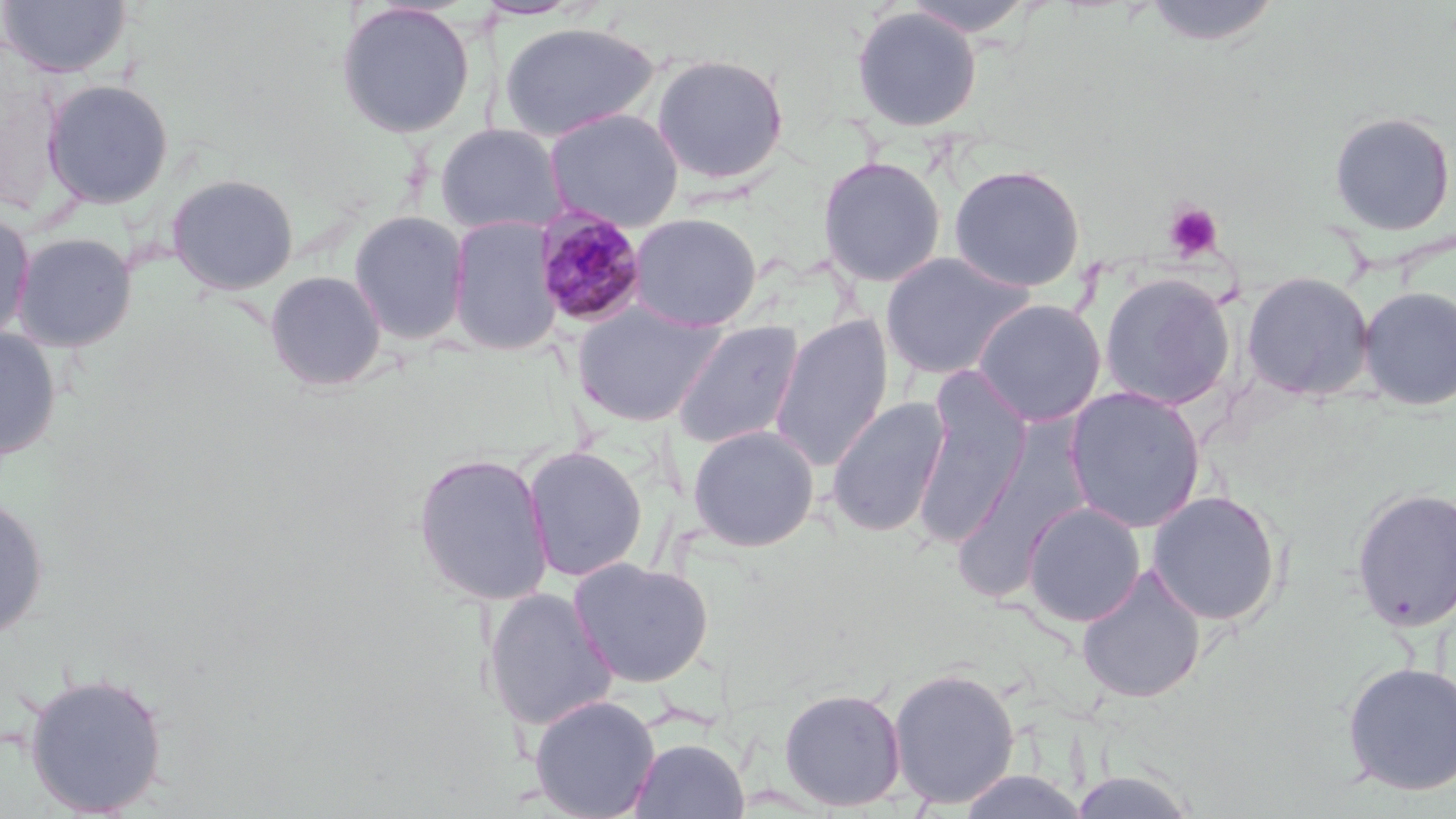

Summary:
  - Coordinate format: approximate bounding boxes as named x1/y1/x2/y2 corners in pixels
  - Platelet locations: (x1=1163, y1=202, x2=1223, y2=261)
  - Plasmodium malariae-infected red blood cell locations: (x1=534, y1=207, x2=648, y2=328)
  - Uninfected red blood cell locations: (x1=0, y1=0, x2=131, y2=78), (x1=899, y1=0, x2=1037, y2=38), (x1=1141, y1=0, x2=1283, y2=47), (x1=334, y1=2, x2=477, y2=139), (x1=851, y1=6, x2=982, y2=132), (x1=497, y1=21, x2=661, y2=142), (x1=651, y1=53, x2=790, y2=186), (x1=42, y1=78, x2=175, y2=209), (x1=544, y1=108, x2=684, y2=232), (x1=1328, y1=111, x2=1455, y2=236), (x1=434, y1=123, x2=568, y2=236), (x1=817, y1=155, x2=946, y2=287), (x1=949, y1=164, x2=1086, y2=292), (x1=166, y1=173, x2=300, y2=295), (x1=0, y1=209, x2=36, y2=347), (x1=348, y1=209, x2=470, y2=346), (x1=628, y1=212, x2=763, y2=331), (x1=447, y1=214, x2=563, y2=355), (x1=11, y1=231, x2=138, y2=353), (x1=879, y1=251, x2=1034, y2=381), (x1=264, y1=270, x2=388, y2=392), (x1=1241, y1=271, x2=1375, y2=401), (x1=1099, y1=273, x2=1236, y2=410), (x1=1358, y1=285, x2=1456, y2=410), (x1=972, y1=298, x2=1107, y2=427), (x1=571, y1=301, x2=724, y2=427), (x1=770, y1=315, x2=894, y2=471), (x1=670, y1=320, x2=805, y2=450), (x1=0, y1=328, x2=61, y2=462), (x1=911, y1=381, x2=1030, y2=547), (x1=1064, y1=387, x2=1205, y2=532), (x1=826, y1=397, x2=950, y2=537), (x1=687, y1=424, x2=821, y2=551), (x1=522, y1=445, x2=648, y2=582), (x1=949, y1=445, x2=1089, y2=602), (x1=411, y1=451, x2=554, y2=607), (x1=1351, y1=486, x2=1456, y2=633), (x1=1147, y1=490, x2=1283, y2=626), (x1=0, y1=494, x2=49, y2=640), (x1=1023, y1=501, x2=1145, y2=627), (x1=568, y1=557, x2=715, y2=688), (x1=1075, y1=565, x2=1207, y2=703), (x1=481, y1=587, x2=618, y2=732), (x1=1341, y1=660, x2=1456, y2=796), (x1=888, y1=666, x2=1021, y2=808), (x1=23, y1=670, x2=169, y2=816), (x1=778, y1=686, x2=907, y2=811), (x1=528, y1=694, x2=661, y2=819), (x1=630, y1=736, x2=749, y2=818), (x1=1067, y1=769, x2=1201, y2=818), (x1=957, y1=770, x2=1089, y2=818)
  - Slide-level diagnosis: Plasmodium malariae
  - Field of view: single
  - Image size: 1456×819 pixels
  - Modality: optical microscopy
  - Preparation: thin blood smear
  - Stain: May-Grünwald-Giemsa
  - Magnification: 1000x